Assess this cell for malaria.
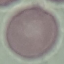

Uninfected.

Summary:
  - Stain: Giemsa
  - Image type: automatically extracted cell patch, resized to 64 × 64 pixels
  - Capture: smartphone through the microscope eyepiece
  - Preparation: thin blood smear